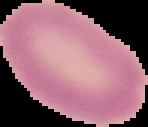 From a thin blood film. Cell region segmented out of the field of view; the surrounding area is masked to black. Malaria status: uninfected. Image is 148×127 pixels.